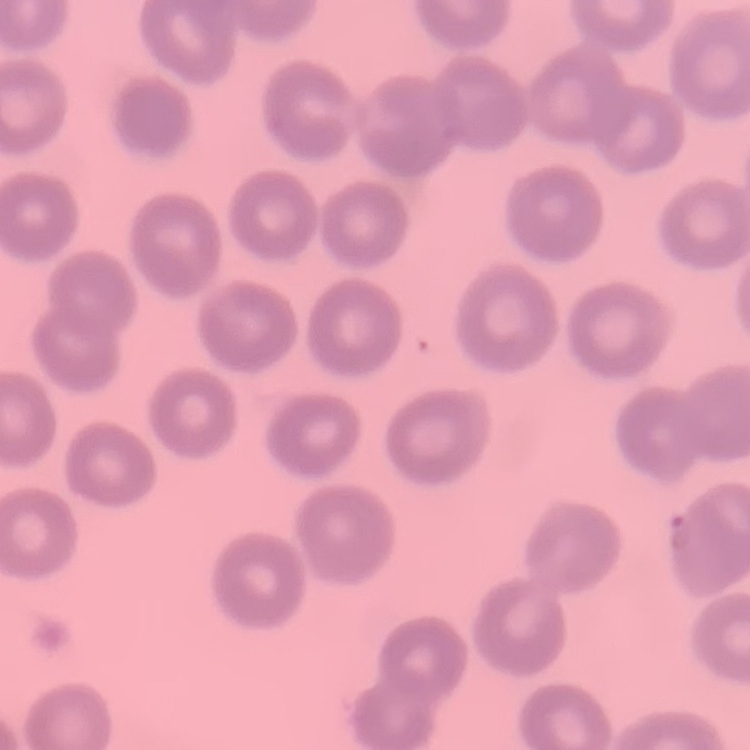

{
  "red_blood_cell_morphology": "no rouleaux formation",
  "preparation": "thin blood smear",
  "image_type": "square crop of a larger photomicrograph",
  "stain": "Field's or Giemsa"
}